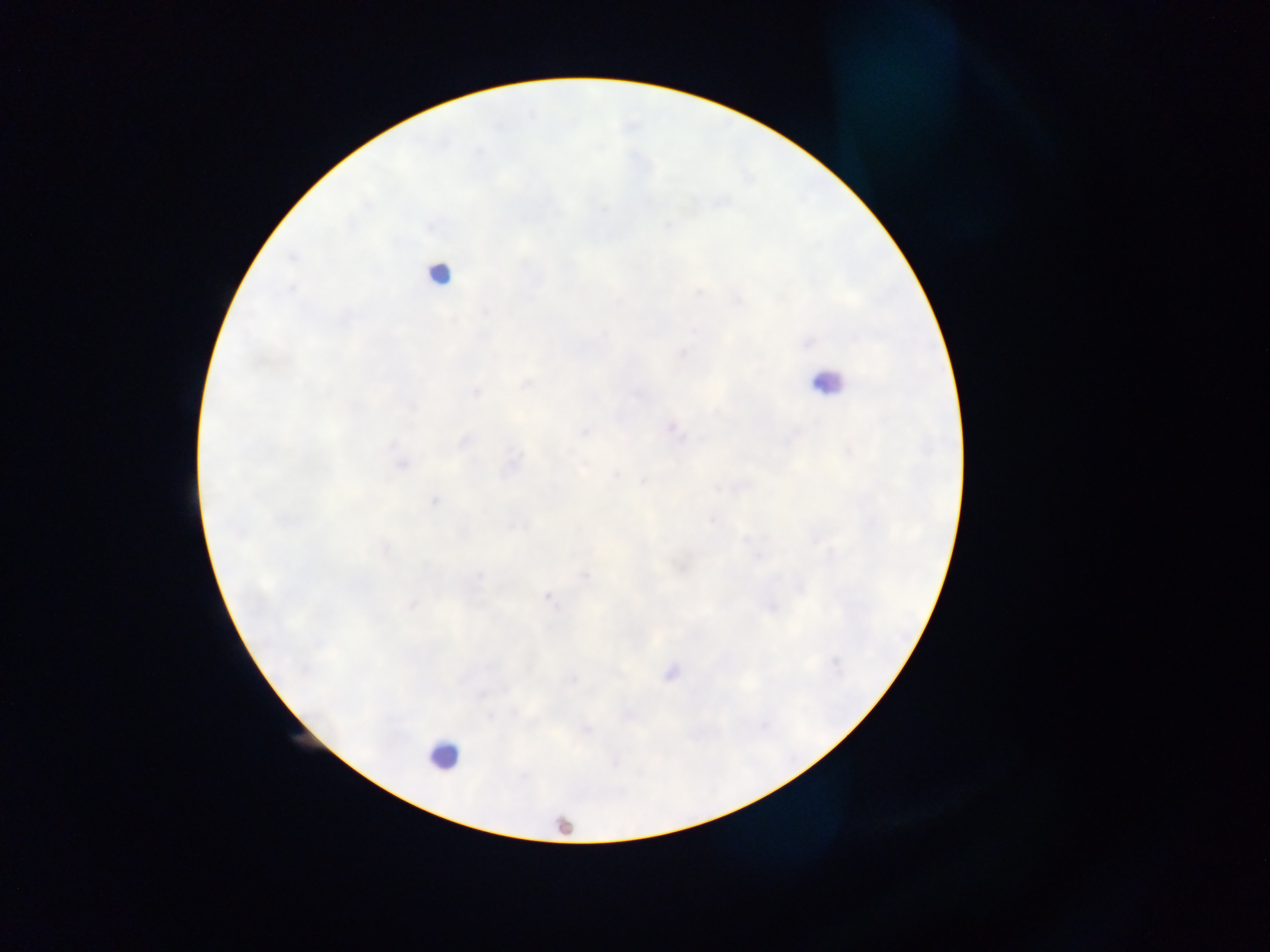

capture: mobile-phone photograph through a microscope
malaria_parasite_locations: 'approximate centers as (x, y) in pixels: (698, 293), (737, 301), (618, 303), (484, 311), (694, 332), (808, 342), (683, 352), (526, 384), (476, 392), (411, 408), (671, 428), (585, 432), (463, 442), (392, 446), (514, 462), (402, 465), (616, 476), (644, 481), (434, 501), (711, 521), (519, 526), (385, 549), (758, 556), (682, 568), (585, 575), (478, 576), (548, 598), (413, 606), (771, 607), (836, 663), (670, 674), (571, 680), (515, 712), (490, 716), (585, 729)'
preparation: thick blood smear
image_size: 1270×952 pixels
field_of_view: single
leukocyte_locations: 'approximate centers as (x, y) in pixels: (438, 273), (826, 383), (442, 756), (563, 827)'
country: Ghana